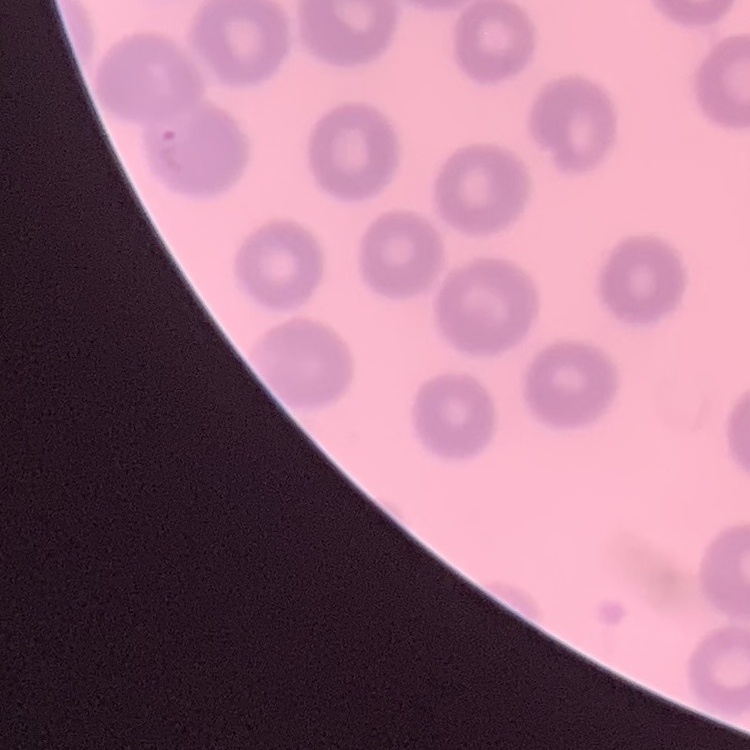
Summary:
  - Erythrocyte morphology: no rouleaux formation
  - Image type: square crop of a larger photomicrograph
  - Stain: Field's or Giemsa
  - Preparation: thin blood film